Give the position of every Plasmodium parasite.
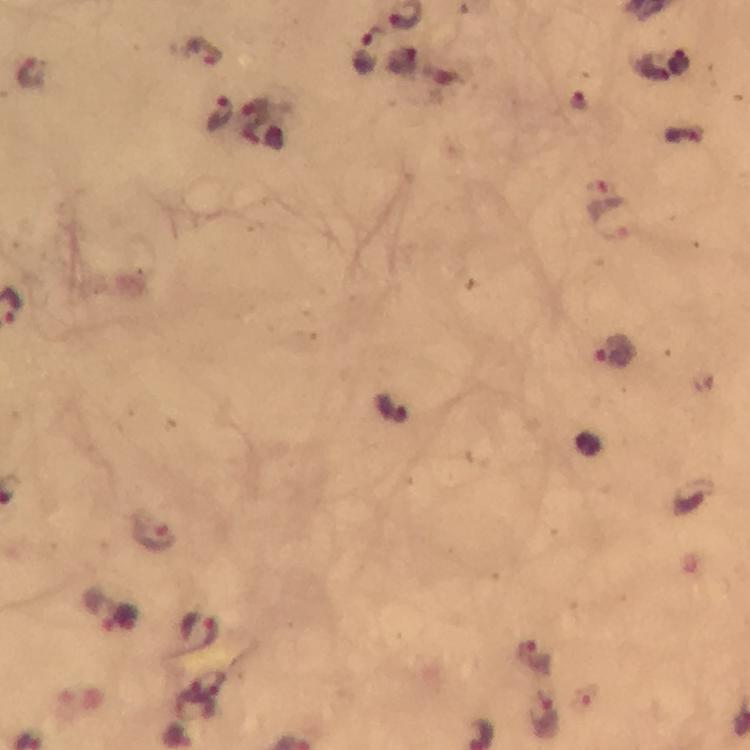

Approximate object centers, in pixels from the top-left corner.
Plasmodium parasites: (x=365, y=52), (x=219, y=115), (x=610, y=220), (x=615, y=351), (x=155, y=530), (x=121, y=619), (x=194, y=636), (x=532, y=657), (x=545, y=716).

Summary:
  - Magnification: 100x
  - Image size: 750×750 pixels
  - Cropped from: one field of view
  - Capture: smartphone camera through the microscope
  - Immersion oil: applied
  - Stain: Giemsa
  - Context: from a diagnostic examination for malaria
  - Preparation: thick blood smear